Report the malaria status of this cell.
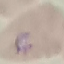

Parasitized.

preparation: thin smear
image_type: cell patch, automatically extracted from a larger field of view and resized to 64 × 64 pixels
capture: smartphone through the microscope eyepiece
stain: Giemsa